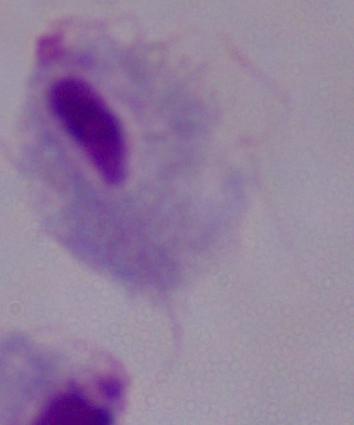
Summary:
  - Magnification: 1000x
  - Modality: photomicrograph
  - Identification: trichomonad